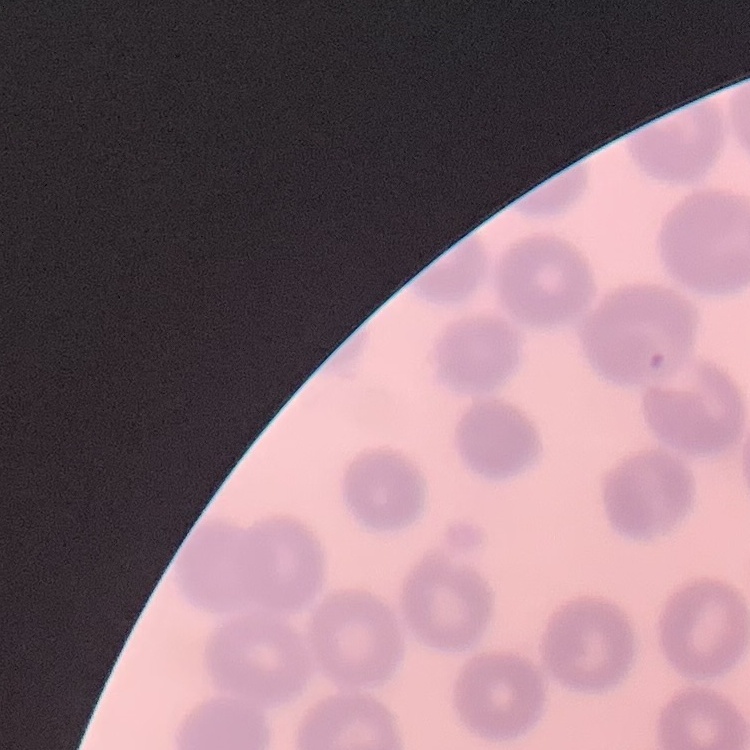

The red blood cells show no rouleaux formation. Thin peripheral smear. Field's or Giemsa stain. Square crop of a larger photomicrograph.